Comment on the morphology of the red blood cells.
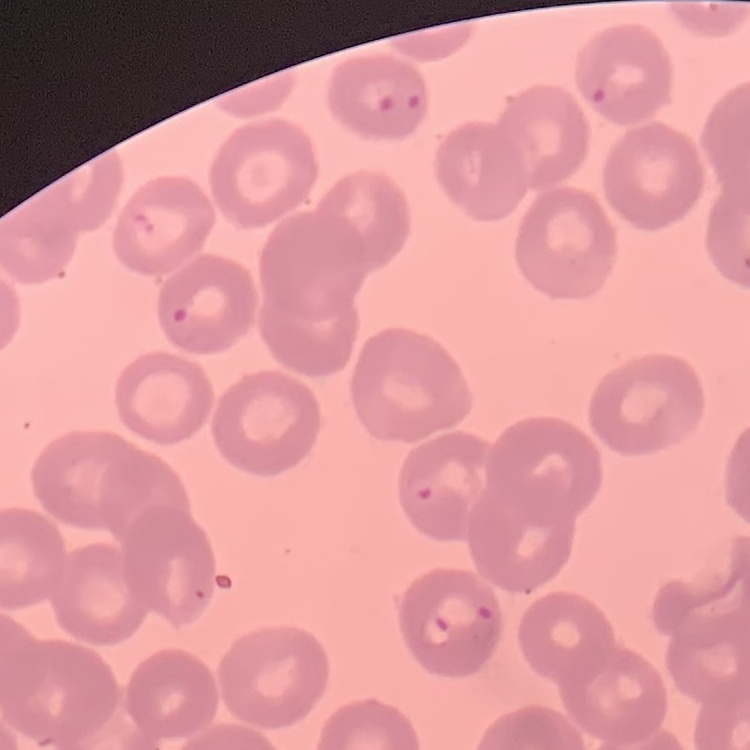

No rouleaux formation.

Square crop of a larger photomicrograph. Field's or Giemsa stain. Thin peripheral smear.